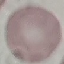
Result: no malaria parasites detected. Cell patch, automatically extracted from a larger field of view and resized to 64 × 64 pixels. Giemsa-stained preparation. Thin blood smear. Acquired by smartphone through the microscope eyepiece.